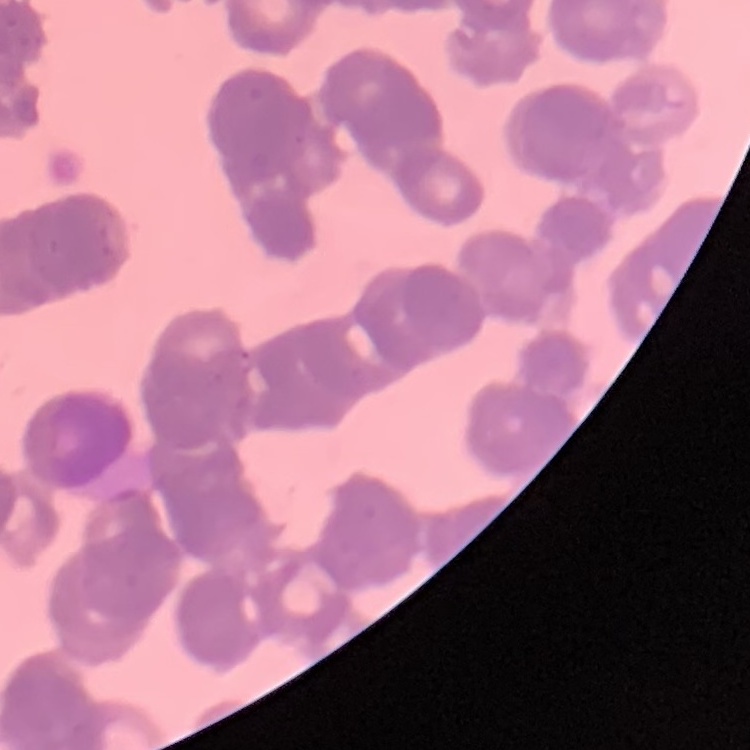

The red blood cells show rouleaux formation. Field's or Giemsa stain. Square crop of a larger photomicrograph. Thin blood film.